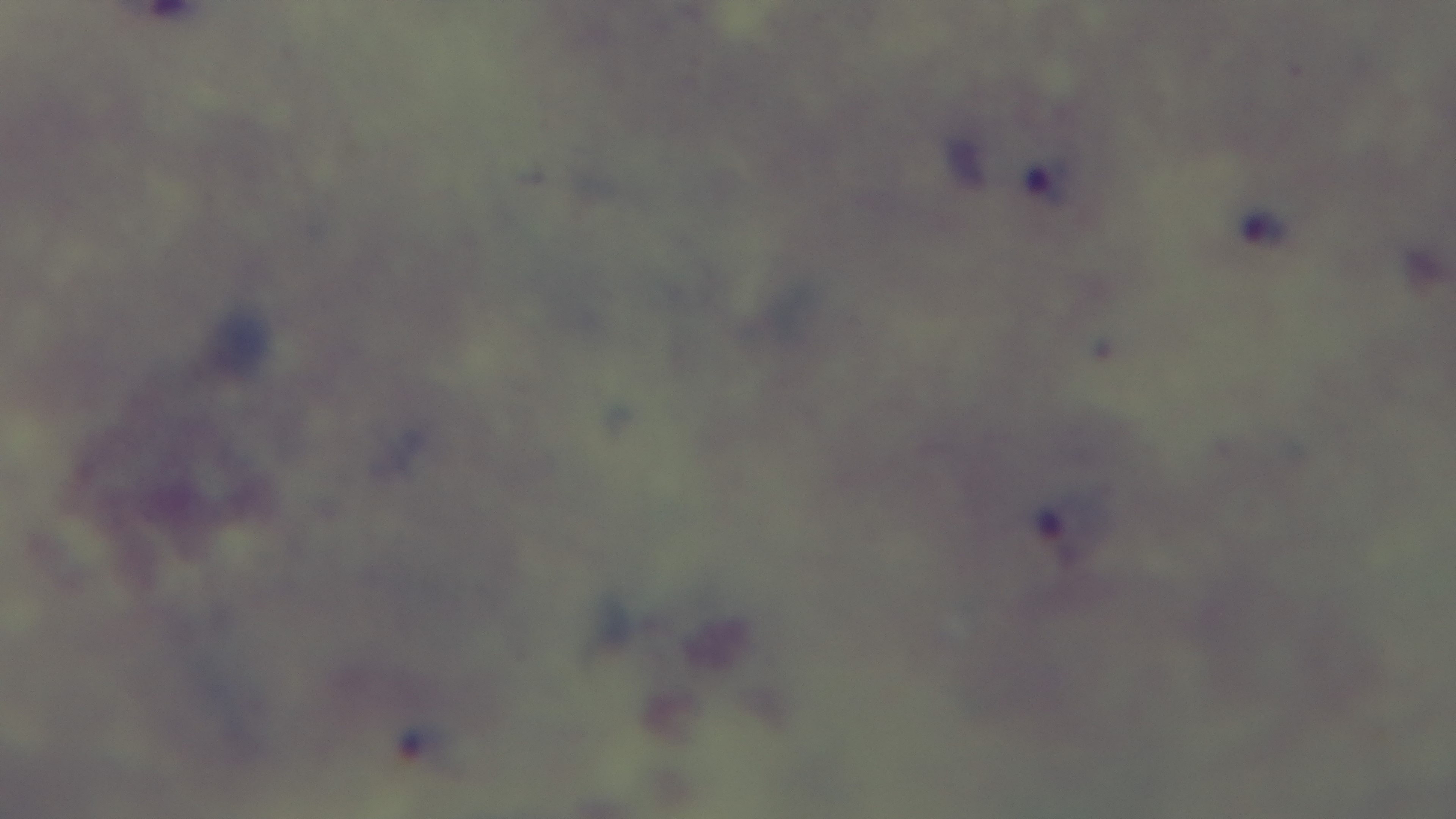
Summary:
  - Malaria status: infected
  - Stain: Giemsa
  - Objective: 100x oil immersion
  - Modality: light microscopy
  - Preparation: thick smear
  - Capture: mounted 4K digital camera
  - Field of view: one from the slide